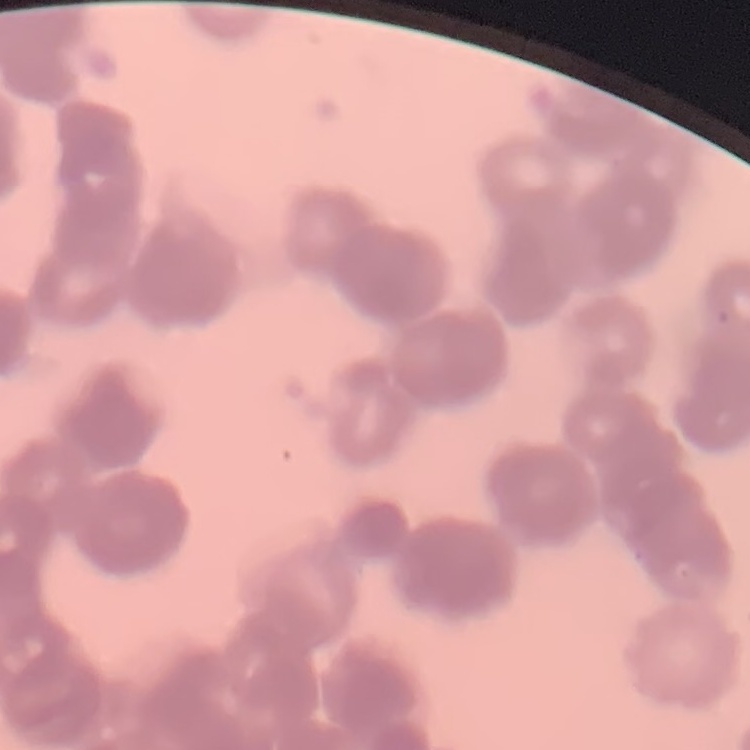

The erythrocytes show rouleaux formation. Thin peripheral smear. Square crop of a larger photomicrograph. Field's or Giemsa stain.